Identify the parasite.
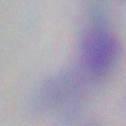
This is Toxoplasma gondii.

Micrograph. Captured at 1000x magnification.